Describe the morphology of the erythrocytes.
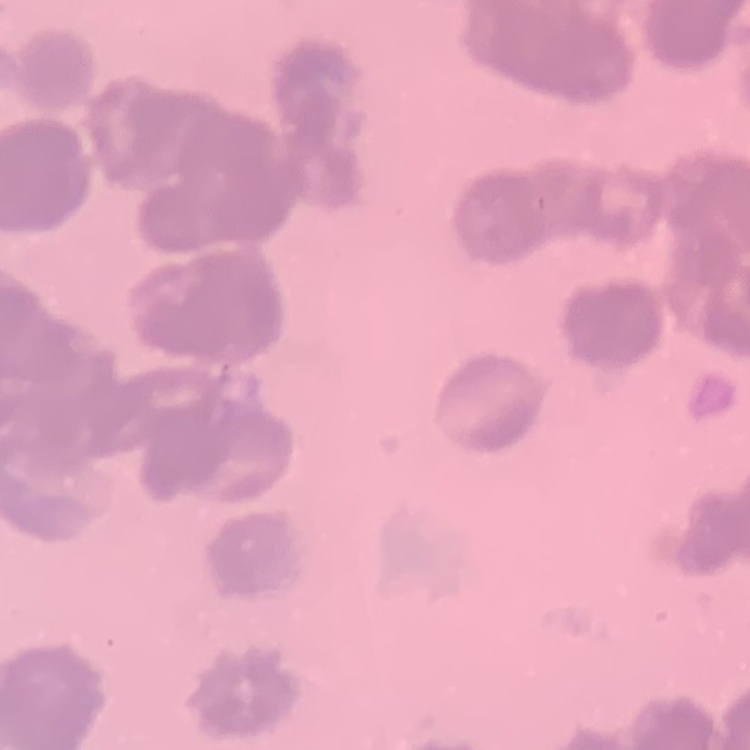
They show rouleaux formation.

Square crop of a larger photomicrograph. Stained with either Field's or Giemsa. Thin peripheral smear.